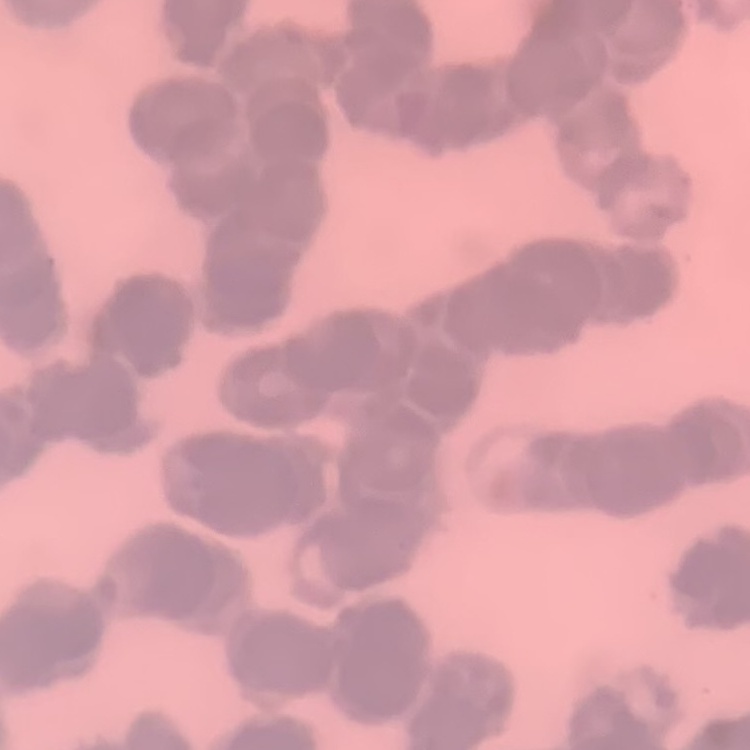

Summary:
  - Red blood cell morphology: rouleaux formation
  - Image type: square crop of a larger photomicrograph
  - Preparation: thin peripheral smear
  - Stain: Field's or Giemsa